State the blood parasite species.
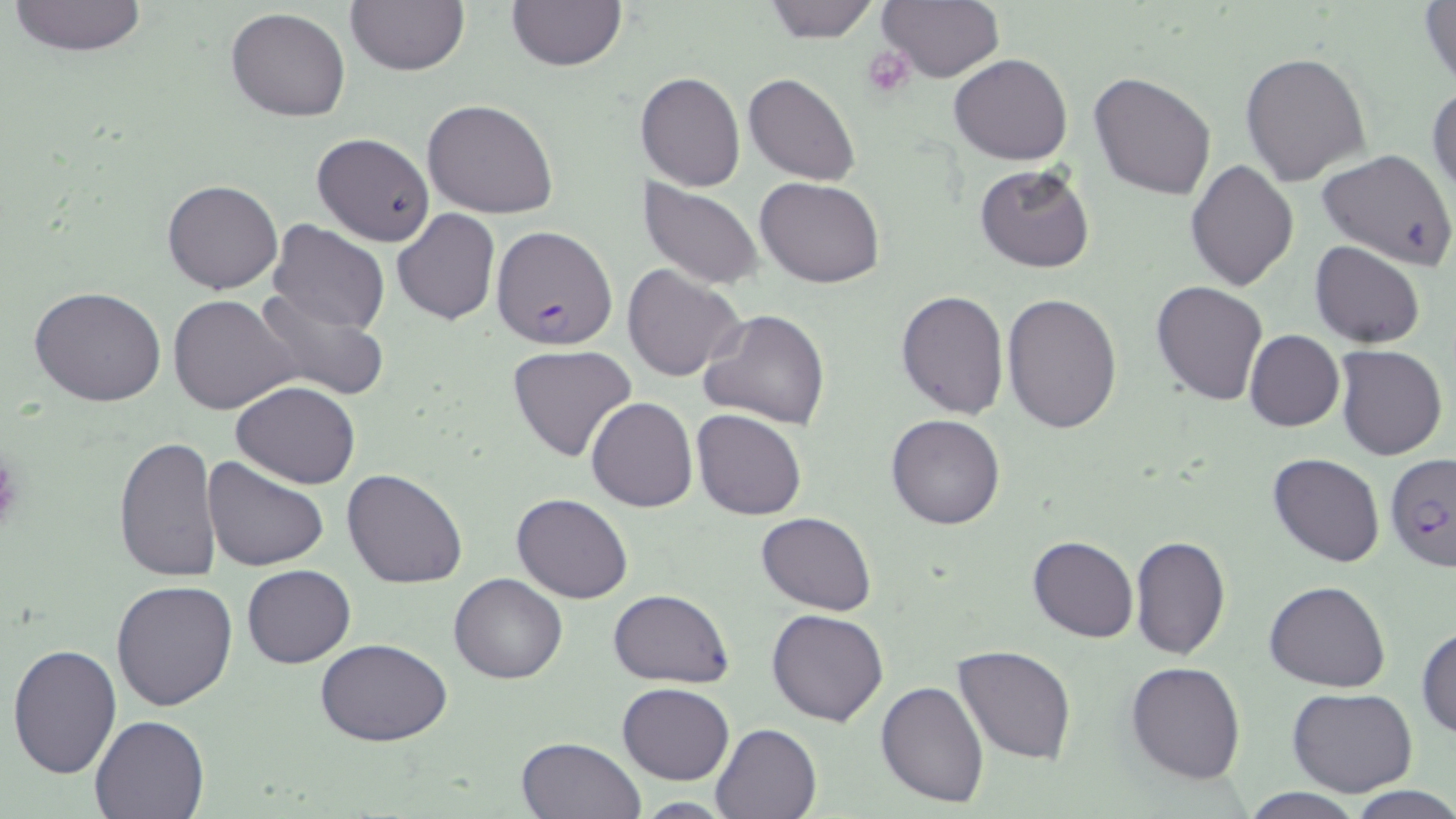

Plasmodium falciparum.

stain: May-Grünwald-Giemsa
field_of_view: one of a larger specimen
platelet_locations: 'approximate bounding boxes as [x1, y1, x2, y2] in pixels: [862, 45, 918, 99], [0, 451, 22, 535]'
modality: optical microscopy
image_size: 1456×819 pixels
magnification: 1000x
plasmodium_falciparum_infected_red_blood_cell_locations: 'approximate bounding boxes as [x1, y1, x2, y2] in pixels: [491, 226, 619, 351], [1385, 450, 1453, 571]'
preparation: thin blood film
uninfected_red_blood_cell_locations: 'approximate bounding boxes as [x1, y1, x2, y2] in pixels: [8, 0, 150, 57], [344, 0, 470, 76], [761, 0, 881, 43], [877, 0, 1005, 83], [506, 1, 626, 71], [1420, 1, 1455, 92], [224, 7, 352, 122], [949, 52, 1073, 165], [1241, 52, 1371, 187], [635, 71, 745, 191], [1089, 71, 1216, 201], [744, 73, 860, 186], [1427, 81, 1456, 201], [423, 99, 559, 220], [311, 133, 434, 245], [1316, 148, 1454, 269], [1186, 159, 1298, 290], [975, 164, 1096, 273], [755, 176, 883, 288], [162, 179, 283, 295], [638, 179, 765, 292], [391, 209, 501, 327], [268, 220, 390, 336], [1309, 240, 1428, 348], [623, 265, 747, 382], [1150, 280, 1268, 405], [29, 286, 169, 407], [251, 287, 390, 401], [896, 289, 1009, 419], [1001, 292, 1124, 433], [167, 293, 301, 415], [698, 308, 831, 429], [1244, 329, 1345, 431], [507, 343, 638, 462], [1336, 345, 1447, 460], [231, 380, 361, 489], [586, 396, 698, 512], [692, 409, 807, 521], [886, 414, 1005, 530], [113, 435, 224, 584], [1268, 453, 1385, 568], [202, 456, 329, 571], [342, 468, 469, 589], [512, 492, 634, 604], [757, 510, 876, 615], [1128, 534, 1230, 660], [1027, 535, 1137, 642], [242, 565, 356, 668], [450, 573, 568, 684], [111, 578, 240, 711], [1264, 580, 1390, 691], [608, 589, 733, 687], [768, 609, 889, 727], [1416, 624, 1456, 740], [315, 638, 452, 747], [7, 644, 122, 780], [953, 645, 1076, 764], [1126, 662, 1247, 784], [876, 679, 990, 806], [617, 682, 736, 784], [1288, 688, 1418, 797], [90, 714, 210, 818], [710, 722, 822, 818], [515, 736, 646, 819], [1345, 785, 1456, 818], [1239, 789, 1368, 819], [631, 798, 740, 816]'